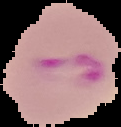
image_type: cell region segmented out of the field of view; surrounding area masked to black
image_size: 121×127 pixels
malaria_status: parasitized
preparation: thin blood smear